Identify the parasite.
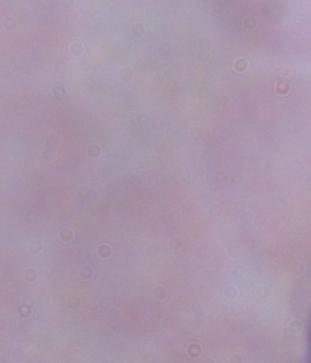

This is a trypanosome.

Micrograph. 1000x magnification.